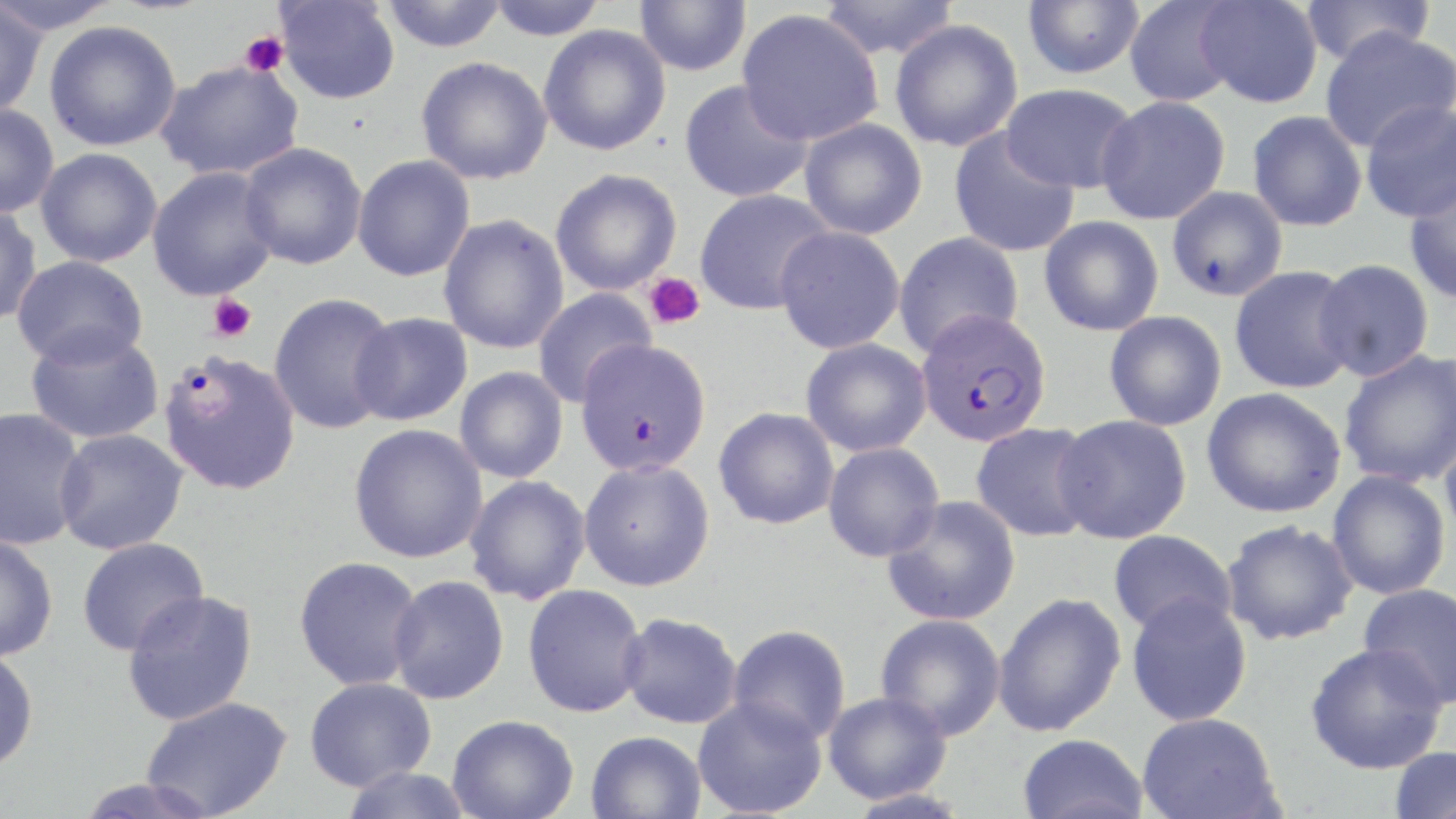

Approximate bounding boxes as (x1, y1, x2, y2) in pixels. Uninfected red blood cell locations: (0, 0, 123, 36), (379, 0, 508, 52), (485, 0, 609, 40), (634, 0, 752, 76), (816, 0, 960, 60), (1023, 0, 1144, 80), (1124, 0, 1242, 107), (1194, 0, 1324, 109), (1300, 0, 1436, 67), (274, 1, 400, 105), (0, 3, 48, 118), (737, 9, 884, 146), (890, 19, 1024, 152), (44, 20, 182, 152), (539, 24, 671, 156), (1319, 26, 1456, 153), (416, 56, 553, 185), (156, 59, 306, 180), (679, 79, 813, 203), (1001, 83, 1139, 194), (1095, 95, 1230, 225), (1359, 99, 1456, 223), (0, 103, 59, 219), (1247, 110, 1367, 232), (799, 118, 928, 240), (948, 128, 1080, 258), (239, 142, 368, 270), (35, 147, 163, 267), (352, 154, 475, 282), (146, 167, 280, 301), (550, 168, 682, 296), (1404, 175, 1456, 306), (1166, 186, 1288, 301), (695, 188, 835, 315), (0, 204, 42, 325), (438, 213, 570, 354), (1040, 215, 1164, 336), (774, 226, 906, 354), (893, 231, 1024, 357), (12, 255, 149, 368), (1312, 258, 1434, 382), (1229, 265, 1359, 394), (532, 287, 656, 408), (268, 292, 398, 435), (1104, 310, 1227, 431), (349, 312, 473, 426), (24, 326, 165, 445), (801, 338, 932, 457), (1338, 349, 1456, 488), (454, 366, 568, 483), (1202, 387, 1346, 518), (0, 407, 89, 550), (714, 407, 839, 529), (1053, 415, 1192, 544), (970, 422, 1099, 542), (349, 423, 489, 563), (53, 429, 188, 555), (1439, 429, 1456, 552), (823, 441, 945, 562), (579, 459, 715, 591), (1327, 470, 1451, 600), (464, 475, 591, 605), (882, 495, 1021, 626), (1221, 518, 1359, 645), (1107, 529, 1237, 637), (0, 534, 58, 662), (77, 536, 209, 655), (293, 556, 426, 691), (387, 575, 510, 704), (1357, 582, 1456, 709), (522, 583, 648, 718), (122, 589, 258, 726), (992, 592, 1126, 736), (1126, 593, 1252, 726), (617, 612, 743, 729), (875, 613, 1006, 740), (727, 624, 851, 745), (1304, 642, 1447, 774), (0, 647, 39, 774), (305, 677, 436, 792), (823, 690, 951, 804), (692, 695, 828, 818), (142, 696, 292, 819), (1136, 712, 1283, 819), (447, 714, 578, 819), (585, 730, 707, 819), (1017, 733, 1149, 819), (1387, 745, 1455, 819), (339, 765, 473, 819), (843, 788, 973, 819). Plasmodium falciparum-infected red blood cell locations: (915, 308, 1053, 447), (575, 339, 712, 476), (158, 350, 301, 495). Platelet locations: (239, 31, 289, 77), (644, 272, 706, 330), (207, 294, 257, 342). Slide-level diagnosis: Plasmodium falciparum. May-Grünwald-Giemsa stain. Light microscopy. Single field of view. Captured at 1000x magnification. Image is 1456×819 pixels. Thin blood smear.